Name the parasite shown.
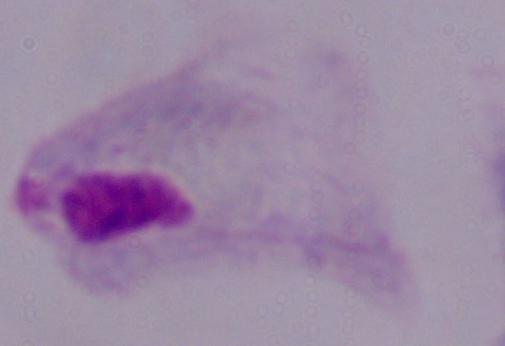

A trichomonad.

Photomicrograph. Captured at 1000x magnification.